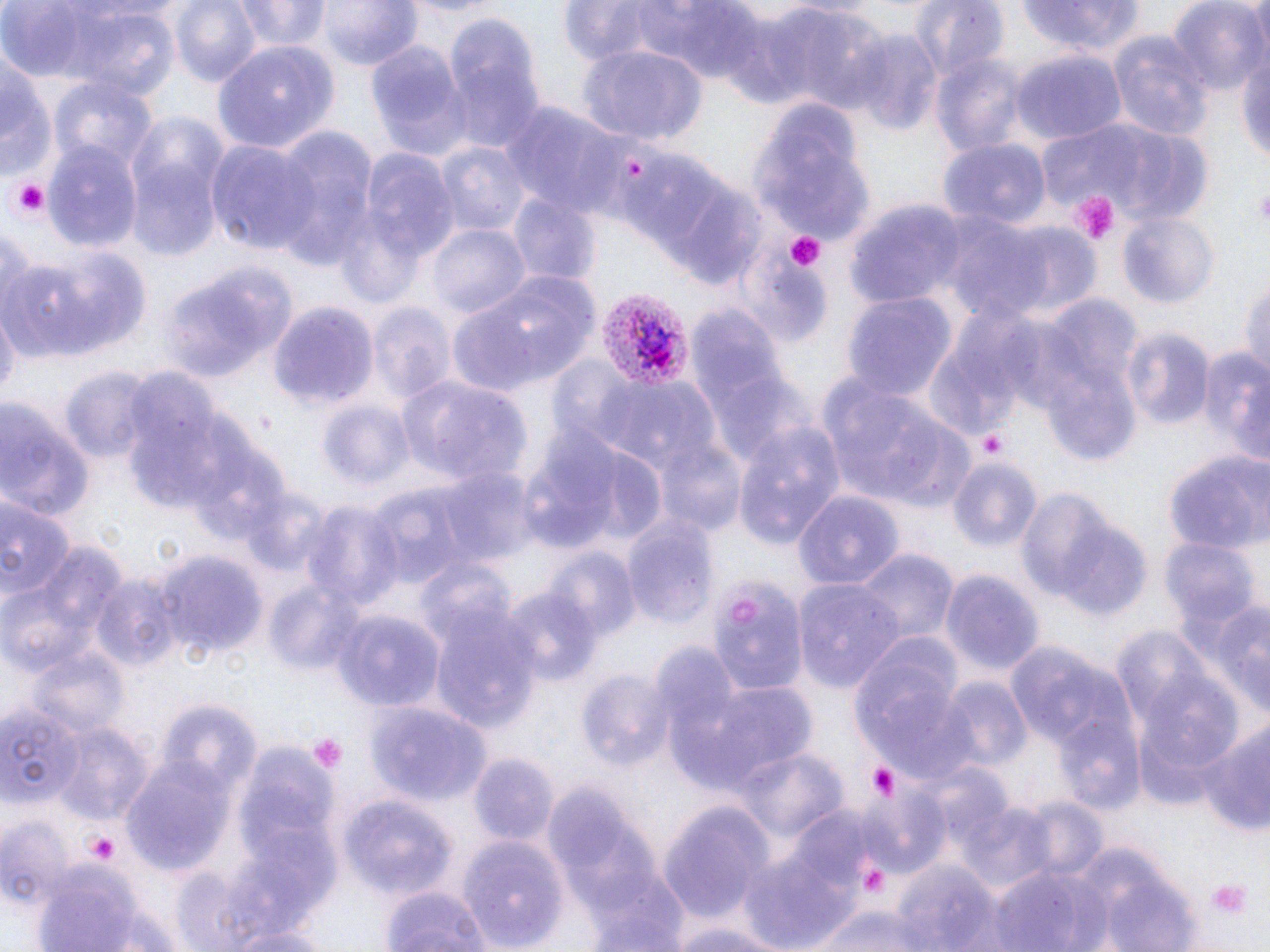

Summary:
  - Coordinate format: approximate bounding boxes as (x1,y1)-(x2,y2) corner pairs in pixels
  - Platelet locations: (10,179)-(52,219), (1252,182)-(1270,225), (1065,189)-(1121,245), (783,230)-(826,272), (977,429)-(1009,460), (307,734)-(346,774), (862,760)-(904,803), (80,827)-(123,865), (1207,878)-(1252,920)
  - Uninfected red blood cell locations: (169,0)-(262,88), (316,0)-(423,72), (1169,0)-(1268,97), (233,1)-(332,52), (913,1)-(1009,86), (0,2)-(147,82), (556,2)-(687,67), (645,2)-(770,84), (1017,2)-(1148,57), (62,6)-(181,102), (771,8)-(892,114), (443,18)-(546,150), (1109,31)-(1216,139), (852,33)-(941,136), (365,37)-(473,159), (1236,39)-(1270,173), (215,41)-(339,154), (579,44)-(707,144), (0,46)-(51,181), (1012,50)-(1127,145), (933,54)-(1029,158), (52,77)-(158,172), (751,98)-(874,244), (503,103)-(627,217), (1057,117)-(1214,230), (270,129)-(378,268), (209,139)-(322,254), (940,139)-(1046,230), (42,141)-(144,253), (437,143)-(531,235), (351,147)-(461,282), (127,160)-(224,262), (657,178)-(768,290), (508,195)-(596,284), (847,202)-(967,306), (940,212)-(1052,324), (1118,213)-(1216,307), (993,221)-(1102,322), (428,222)-(529,321), (0,226)-(37,322), (21,248)-(151,362), (5,262)-(92,360), (452,268)-(599,395), (1241,274)-(1270,382), (843,293)-(957,404), (367,301)-(457,404), (268,302)-(379,410), (689,308)-(798,454), (1,312)-(18,404), (1121,329)-(1215,432), (1197,345)-(1270,456), (59,365)-(157,460), (815,372)-(971,514), (400,376)-(532,487), (116,380)-(242,512), (0,400)-(94,525), (317,400)-(416,488), (736,421)-(844,547), (518,426)-(638,554), (187,428)-(297,546), (651,437)-(748,534), (1165,451)-(1268,552), (947,458)-(1040,550), (435,468)-(536,569), (795,488)-(904,592), (1013,489)-(1128,604), (0,496)-(72,609), (302,501)-(398,610), (620,508)-(720,631), (1057,527)-(1153,621), (1163,539)-(1260,629), (0,543)-(122,677), (854,549)-(959,643), (549,551)-(639,643), (158,552)-(268,661), (939,569)-(1043,678), (265,578)-(366,676), (795,578)-(902,692), (90,579)-(179,673), (708,584)-(810,697), (503,587)-(600,684), (1185,595)-(1270,712), (331,607)-(445,711), (430,607)-(540,732), (1001,641)-(1130,755), (852,642)-(972,774), (28,649)-(128,740), (578,671)-(674,769), (684,678)-(820,796), (942,679)-(1031,771), (154,700)-(258,800), (0,703)-(81,805), (368,704)-(491,804), (1198,720)-(1270,836), (57,723)-(152,824), (1057,724)-(1147,815), (737,747)-(846,842), (468,755)-(556,846), (123,759)-(236,872), (855,790)-(951,879), (343,797)-(458,897), (657,803)-(776,920), (961,803)-(1059,893), (790,809)-(873,892), (1,813)-(75,907), (458,836)-(566,951), (742,843)-(859,950), (1072,848)-(1199,951), (893,859)-(1002,952), (989,859)-(1115,952), (32,862)-(150,950), (583,867)-(694,952), (380,883)-(494,952), (812,905)-(933,952), (98,907)-(184,951), (665,917)-(794,952), (219,924)-(337,952)
  - Plasmodium vivax-infected red blood cell locations: (594,289)-(692,393)
  - Slide-level diagnosis: Plasmodium vivax
  - Image size: 1270×952 pixels
  - Field of view: single
  - Modality: light microscopy
  - Stain: May-Grünwald-Giemsa
  - Preparation: thin blood film
  - Magnification: 1000x